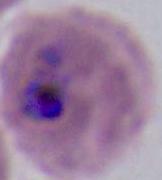
modality = micrograph
magnification = 400x or 1000x
identification = Plasmodium